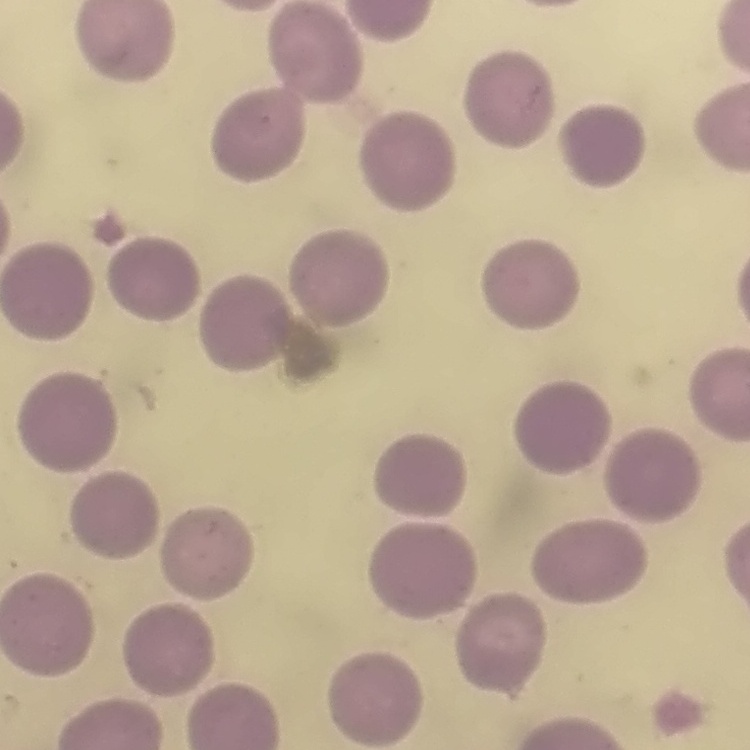
red blood cell morphology = no rouleaux formation
preparation = thin blood smear
stain = Field's or Giemsa
image type = one tile cut from a larger photomicrograph